State which cell type is depicted.
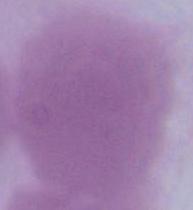
This is an erythrocyte.

modality = photomicrograph
magnification = 1000x